State the blood parasite species.
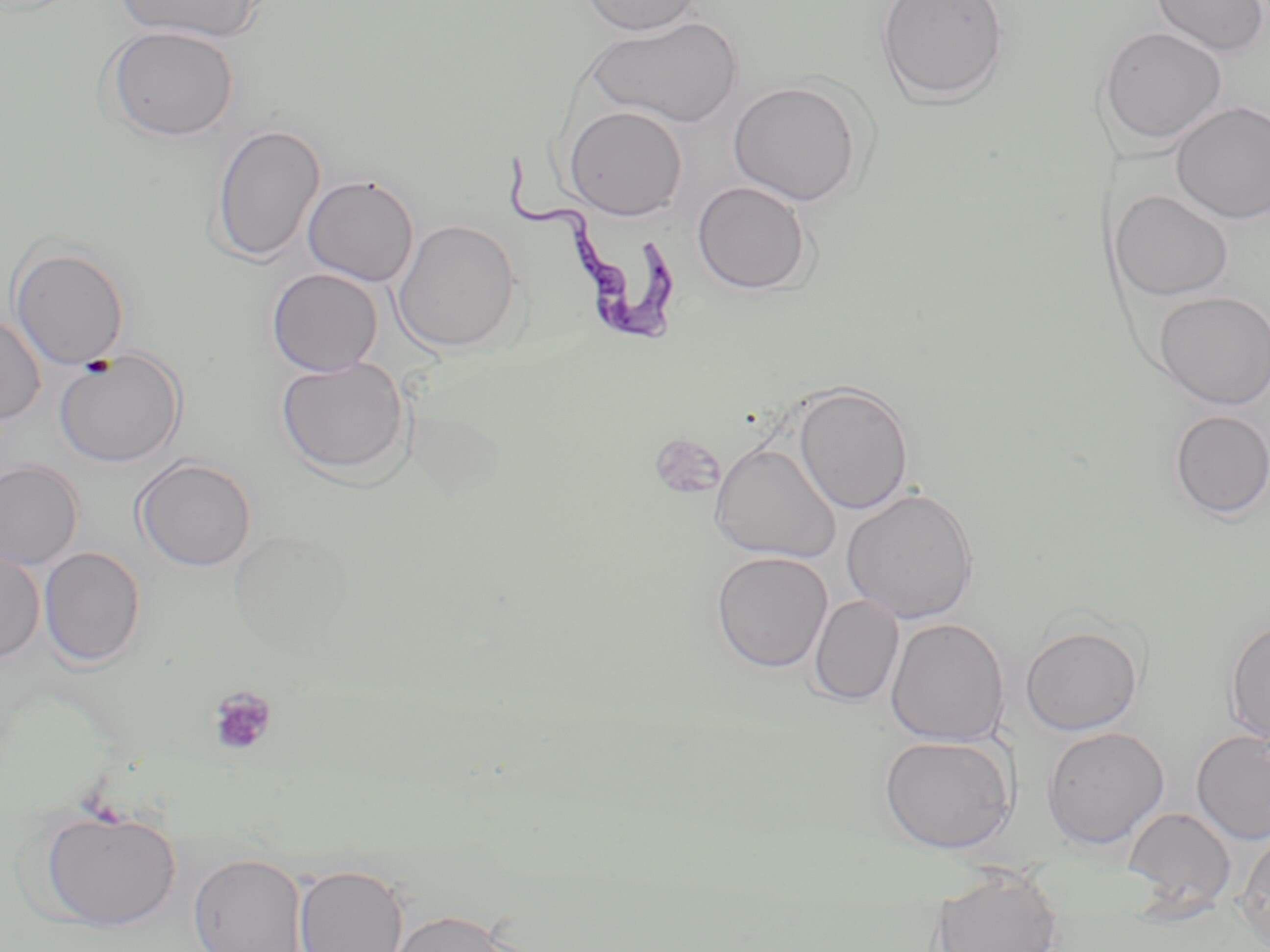
Trypanosoma brucei.

Summary:
  - Coordinate format: approximate bounding boxes as [x1, y1, x2, y2] in pixels
  - Platelet locations: [79, 356, 116, 380], [206, 686, 277, 757]
  - Uninfected red blood cell locations: [115, 0, 265, 43], [578, 0, 702, 36], [874, 0, 1012, 107], [1151, 0, 1270, 58], [585, 15, 743, 128], [102, 25, 240, 142], [1095, 26, 1227, 149], [727, 80, 866, 206], [1170, 100, 1270, 224], [563, 105, 688, 221], [210, 123, 326, 264], [303, 173, 419, 286], [692, 180, 814, 295], [1111, 190, 1233, 301], [393, 219, 524, 354], [10, 243, 130, 370], [266, 267, 384, 377], [1154, 291, 1270, 408], [0, 314, 46, 425], [54, 349, 186, 468], [275, 356, 411, 480], [792, 382, 915, 515], [1167, 409, 1270, 521], [709, 441, 841, 562], [134, 456, 257, 572], [0, 459, 84, 570], [841, 488, 980, 624], [228, 530, 354, 654], [39, 547, 146, 667], [0, 548, 45, 664], [711, 551, 833, 673], [809, 594, 903, 707], [885, 617, 1010, 746], [1222, 617, 1270, 746], [1020, 623, 1145, 736], [1041, 726, 1169, 851], [1191, 729, 1270, 845], [878, 734, 1017, 853], [37, 806, 182, 931], [1122, 806, 1236, 913], [1235, 830, 1270, 946], [188, 852, 308, 952], [293, 863, 410, 952], [928, 865, 1064, 952], [384, 908, 523, 952]
  - Trypanosoma brucei locations: [503, 158, 684, 347]
  - Magnification: 1000x
  - Preparation: thin blood smear
  - Stain: May-Grünwald-Giemsa
  - Field of view: single
  - Modality: optical microscopy
  - Image size: 1270×952 pixels